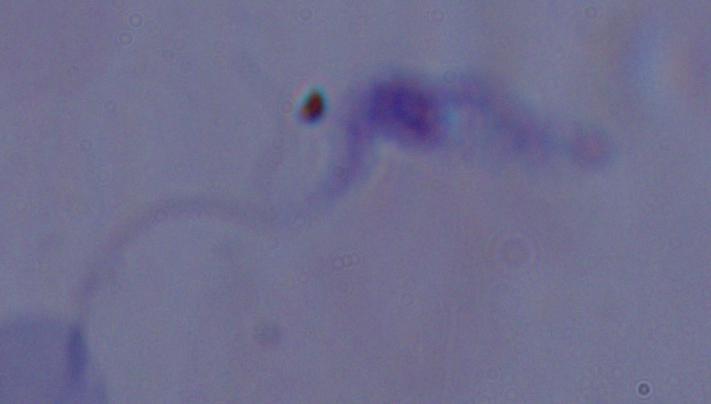
identification = trypanosome
modality = micrograph
magnification = 1000x